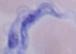 Micrograph. Captured at 1000x magnification. A trypanosome is shown.